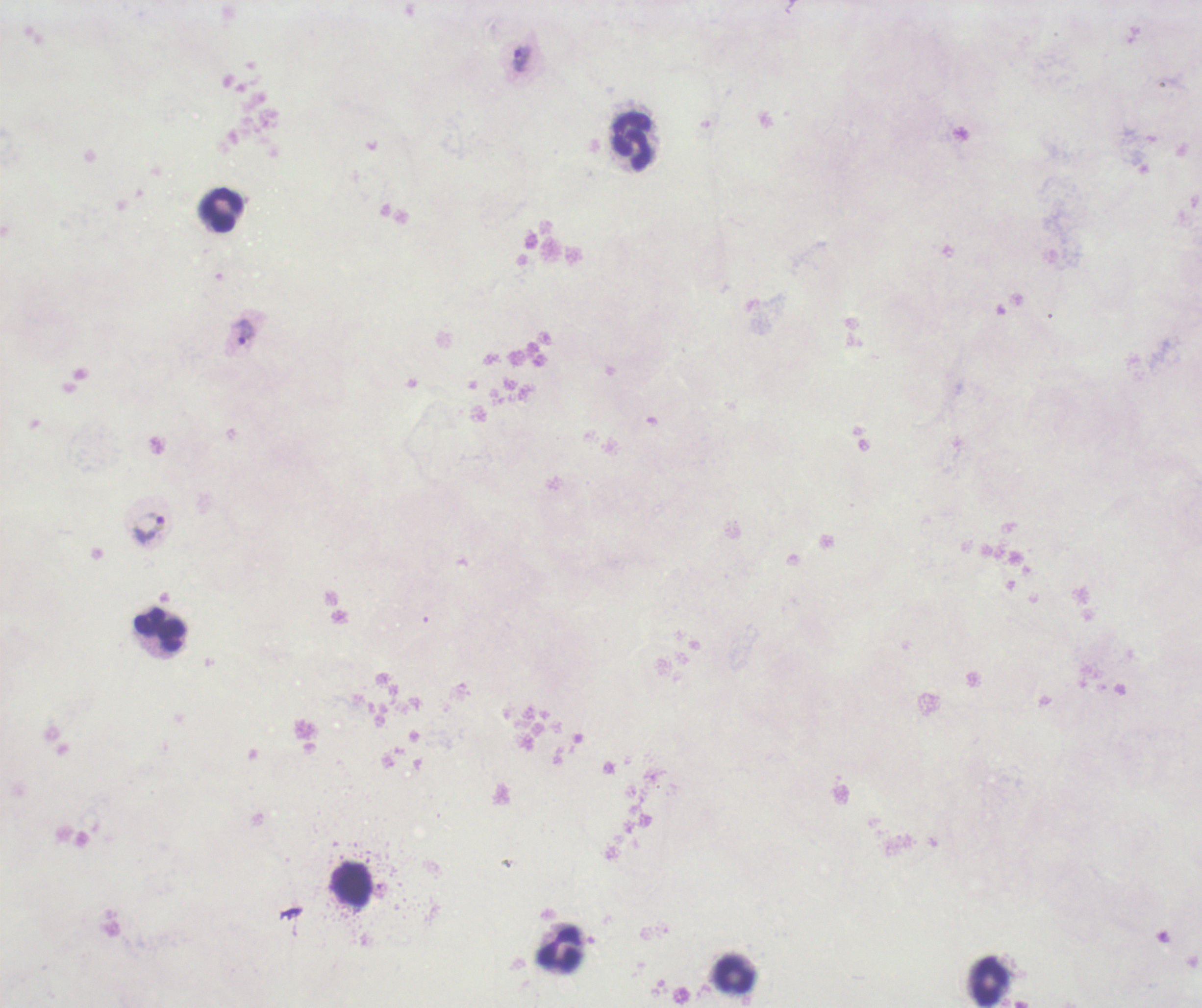
Approximate centers as (x, y) in pixels.
Summary:
  - Trophozoite locations: (521, 58), (245, 331), (148, 527)
  - Leukocyte locations: (631, 141), (221, 210), (159, 630), (352, 884), (558, 949), (732, 976), (988, 982)
  - Background quality: unsatisfactory
  - Result: positive for Plasmodium parasites
  - Coloration quality: bad
  - Stain: Romanowsky
  - Preparation: thick blood film
  - Field of view: one from this slide
  - Context: previously used in a real diagnosis
  - Magnification: 100x
  - Image size: 1202×1008 pixels